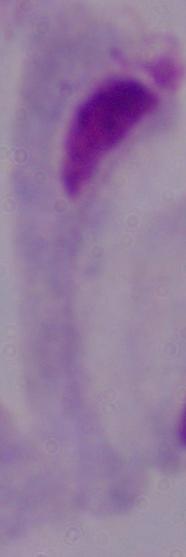

identification: trichomonad
magnification: 1000x
modality: micrograph